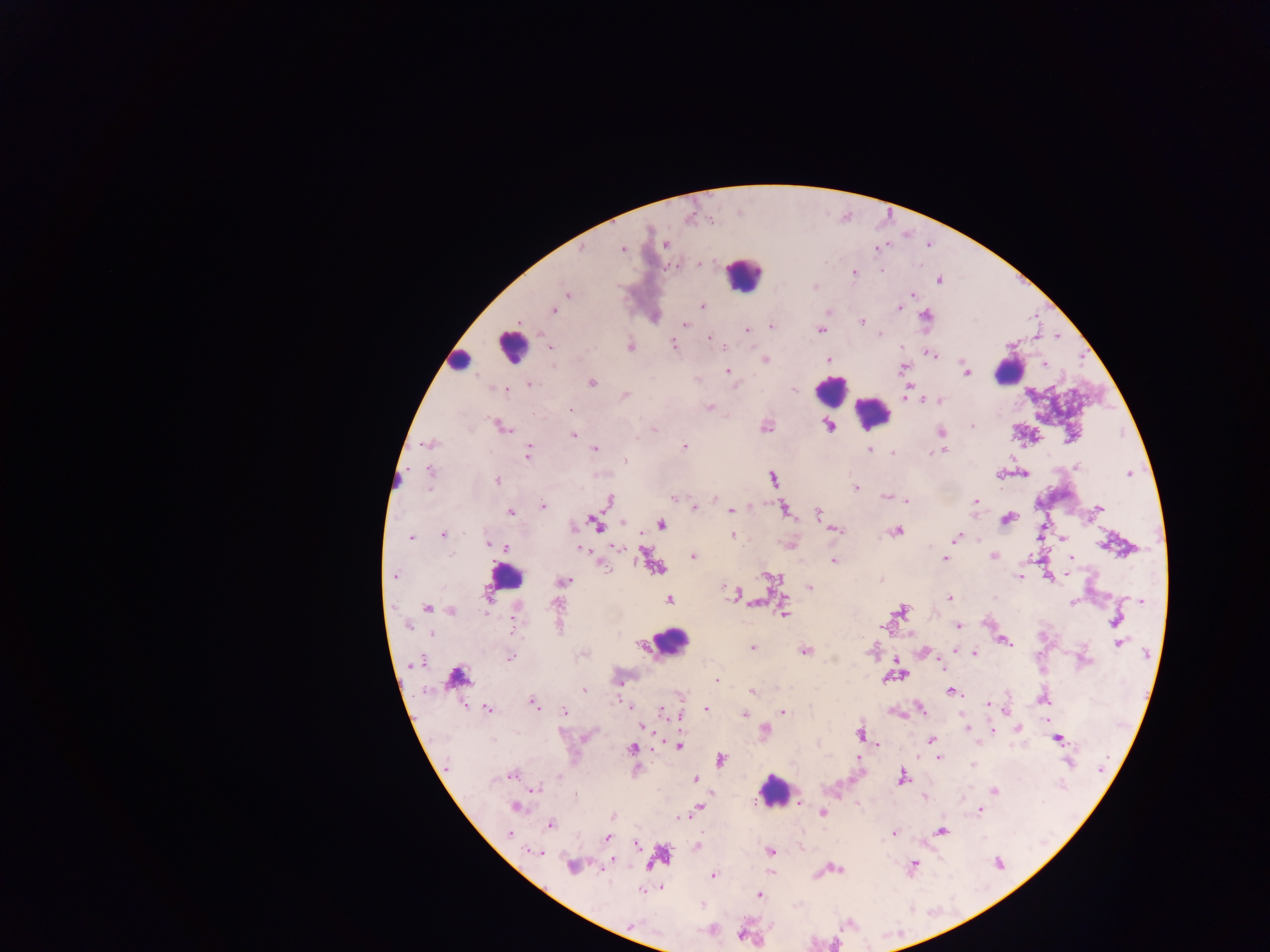
leukocyte_locations: 'approximate centers as (x, y) in pixels: (742, 274), (511, 346), (459, 360), (1009, 370), (831, 390), (873, 414), (399, 479), (504, 578), (671, 642), (773, 790)'
field_of_view: single
capture: mobile-phone photograph through a microscope
preparation: thick blood film
image_size: 1270×952 pixels
country: Ghana
malaria_parasite_locations: 'approximate centers as (x, y) in pixels: (665, 244), (621, 248), (876, 248), (582, 249), (699, 264), (673, 265), (853, 272), (938, 279), (814, 286), (567, 294), (911, 294), (701, 306), (899, 308), (553, 310), (829, 310), (654, 315), (925, 317), (861, 322), (685, 324), (771, 326), (747, 329), (821, 329), (879, 334), (1035, 336), (709, 337), (1058, 337), (672, 344), (629, 346), (550, 347), (930, 355), (828, 358), (764, 360), (1045, 364), (903, 367), (727, 370), (965, 372), (591, 382), (528, 384), (907, 389), (505, 390), (793, 391), (625, 395), (938, 399), (929, 400), (709, 407), (568, 408), (828, 424), (500, 426), (765, 426), (972, 426), (654, 428), (940, 431), (574, 435), (428, 444), (684, 448), (594, 449), (869, 450), (941, 450), (527, 451), (893, 453), (625, 462), (1078, 467), (429, 469), (1130, 472), (1023, 473), (1001, 474), (773, 479), (497, 480), (854, 487), (714, 496), (887, 496), (674, 497), (608, 501), (906, 501), (973, 502), (542, 506), (694, 508), (1099, 508), (784, 509), (730, 510), (511, 512), (818, 513), (1006, 519), (622, 522), (597, 523), (660, 524), (834, 529), (896, 531), (442, 534), (732, 534), (410, 538), (955, 538), (1061, 539), (488, 543), (789, 544), (615, 546), (580, 547), (505, 548), (692, 556), (994, 556), (945, 558), (1069, 558), (834, 560), (651, 561), (603, 565), (658, 567), (394, 575), (1067, 575), (770, 576), (1048, 576), (1021, 577), (562, 581), (724, 587), (809, 587), (733, 593), (948, 597), (1140, 599), (667, 600), (1073, 602), (752, 603), (558, 605), (427, 608), (450, 610), (899, 610), (783, 614), (1116, 620), (988, 623), (407, 625), (958, 626), (513, 628), (431, 633), (909, 633), (1004, 641), (1119, 643), (750, 647), (804, 650), (923, 651), (582, 652), (974, 653), (510, 656), (417, 661), (897, 663), (941, 666), (901, 674), (455, 677), (885, 677), (716, 679), (584, 690), (951, 691), (752, 692), (1042, 697), (987, 702), (532, 703), (630, 706), (486, 708), (705, 708), (921, 709), (661, 710), (564, 711), (783, 711), (1005, 711), (896, 712), (668, 713), (743, 714), (680, 717), (1046, 720), (641, 726), (966, 727), (1017, 727), (992, 729), (764, 731), (859, 734), (585, 737), (1058, 738), (931, 741), (978, 742), (878, 744), (678, 745), (631, 749), (939, 757), (720, 759), (859, 759), (1069, 762), (972, 765), (445, 768), (510, 774), (901, 777), (694, 779), (535, 788), (995, 790), (575, 794), (924, 797), (797, 802), (515, 806), (700, 807), (980, 810), (822, 812), (613, 816), (550, 824), (941, 831), (894, 833), (510, 834), (607, 837), (637, 844), (697, 846), (769, 851), (534, 852), (659, 857), (611, 862), (912, 864), (572, 866), (836, 868), (713, 876), (662, 886), (642, 890), (758, 894), (631, 925), (710, 930), (740, 935)'